Assess this cell for malaria.
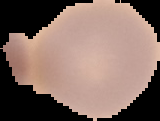

Uninfected.

Cell region segmented out of the field of view; the surrounding area is masked to black. Image is 160×121 pixels. From a thin blood film.